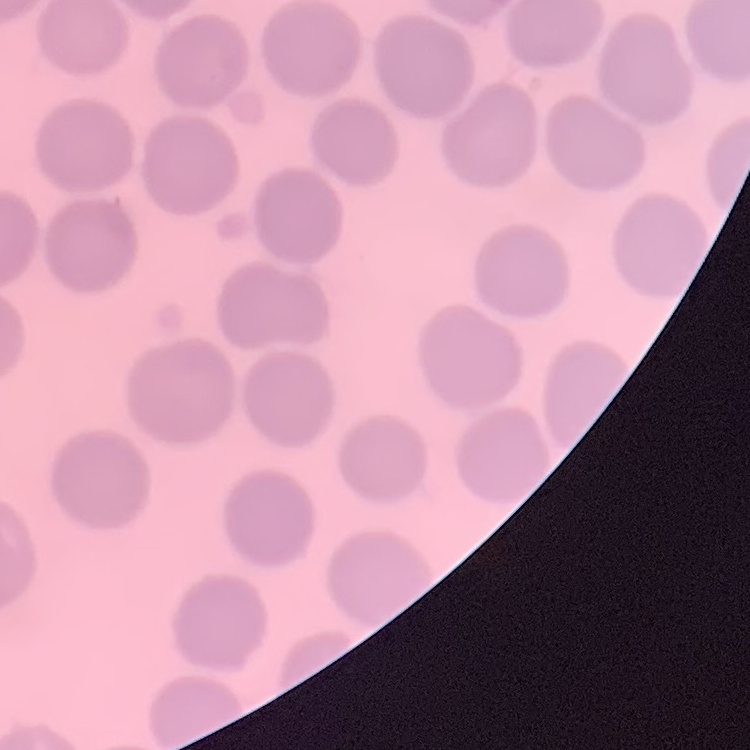

Summary:
  - Red blood cell morphology: no rouleaux formation
  - Preparation: thin blood smear
  - Image type: square crop of a larger photomicrograph
  - Stain: Field's or Giemsa